Give the extent of all Plasmodium ovale-infected red blood cells.
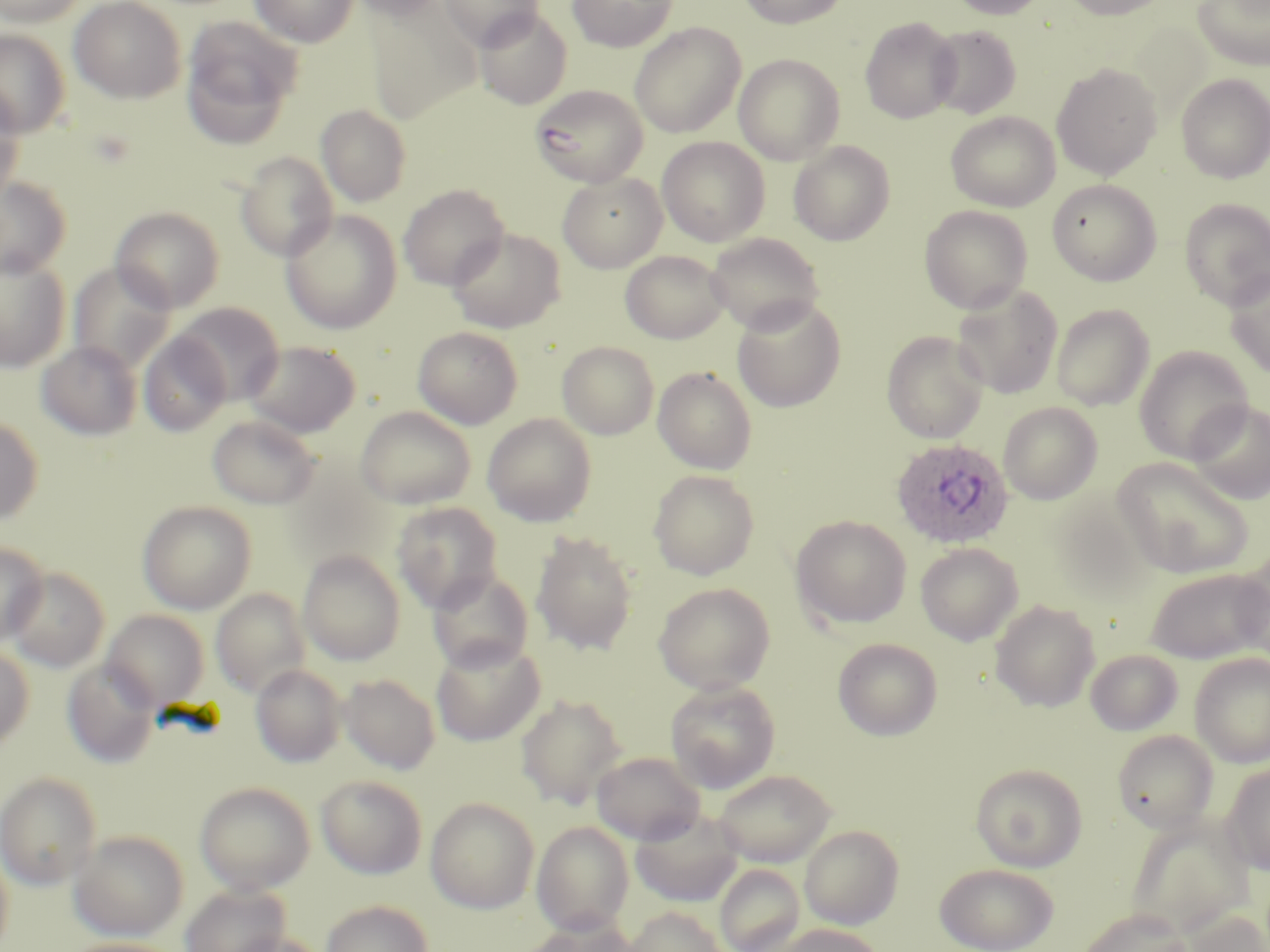

Approximate bounding boxes as [x1, y1, x2, y2] in pixels.
Plasmodium ovale-infected red blood cells: [890, 438, 1014, 548].

Summary:
  - Uninfected red blood cell locations: [69, 0, 186, 103], [249, 0, 358, 48], [348, 0, 447, 22], [440, 0, 545, 51], [567, 0, 677, 51], [736, 0, 853, 28], [946, 0, 1050, 20], [1059, 0, 1174, 20], [1192, 0, 1270, 71], [0, 1, 90, 28], [364, 6, 481, 123], [474, 8, 572, 110], [860, 15, 961, 123], [181, 17, 302, 147], [629, 22, 746, 138], [927, 24, 1021, 119], [0, 29, 70, 138], [733, 53, 845, 165], [1051, 63, 1162, 180], [1176, 73, 1270, 183], [530, 85, 649, 187], [0, 86, 25, 203], [316, 104, 411, 207], [945, 111, 1060, 212], [657, 137, 769, 246], [789, 140, 895, 245], [235, 151, 337, 262], [557, 172, 667, 273], [0, 177, 71, 279], [1047, 179, 1162, 286], [398, 185, 509, 290], [1180, 198, 1270, 309], [919, 205, 1033, 313], [111, 206, 225, 313], [281, 208, 402, 334], [447, 227, 566, 333], [705, 232, 824, 334], [620, 250, 730, 343], [0, 253, 70, 372], [68, 262, 176, 374], [1224, 268, 1270, 380], [951, 284, 1063, 399], [732, 297, 846, 412], [172, 302, 284, 405], [1051, 304, 1154, 411], [413, 326, 523, 429], [881, 330, 989, 444], [138, 332, 231, 435], [242, 340, 361, 437], [36, 341, 142, 440], [557, 341, 659, 439], [1134, 346, 1252, 465], [653, 366, 757, 474], [1186, 399, 1270, 505], [998, 402, 1103, 505], [355, 406, 476, 509], [207, 414, 321, 509], [482, 414, 597, 526], [0, 415, 43, 526], [1112, 458, 1254, 579], [648, 469, 759, 580], [137, 500, 257, 614], [391, 502, 503, 613], [791, 515, 912, 629], [531, 530, 638, 656], [0, 541, 48, 645], [915, 542, 1023, 646], [297, 549, 405, 666], [1235, 552, 1270, 666], [5, 567, 110, 672], [1145, 567, 1268, 664], [427, 569, 534, 673], [653, 583, 775, 695], [211, 589, 311, 698], [990, 599, 1100, 712], [102, 610, 209, 710], [833, 637, 943, 740], [429, 638, 545, 746], [0, 644, 34, 750], [1085, 649, 1183, 736], [1189, 653, 1270, 767], [62, 659, 161, 769], [250, 664, 346, 768], [340, 673, 440, 774], [665, 680, 780, 793], [516, 694, 628, 809], [1113, 730, 1218, 833], [591, 751, 706, 845], [1221, 762, 1270, 875], [971, 764, 1087, 871], [712, 768, 837, 867], [0, 772, 102, 889], [316, 775, 427, 879], [194, 781, 316, 894], [425, 796, 540, 913], [630, 808, 745, 908], [1127, 817, 1254, 937], [532, 821, 635, 935], [800, 824, 904, 929], [69, 830, 188, 941], [0, 845, 14, 952], [935, 862, 1059, 952], [714, 864, 805, 952], [180, 883, 291, 952], [320, 899, 434, 952], [624, 906, 726, 952], [1079, 908, 1192, 952], [1184, 908, 1270, 951], [520, 917, 642, 952], [765, 923, 885, 952], [224, 932, 328, 952], [60, 938, 186, 952]
  - Slide-level diagnosis: Plasmodium ovale
  - Field of view: single
  - Stain: May-Grünwald-Giemsa
  - Preparation: thin blood film
  - Magnification: 1000x
  - Modality: light microscopy
  - Image size: 1270×952 pixels